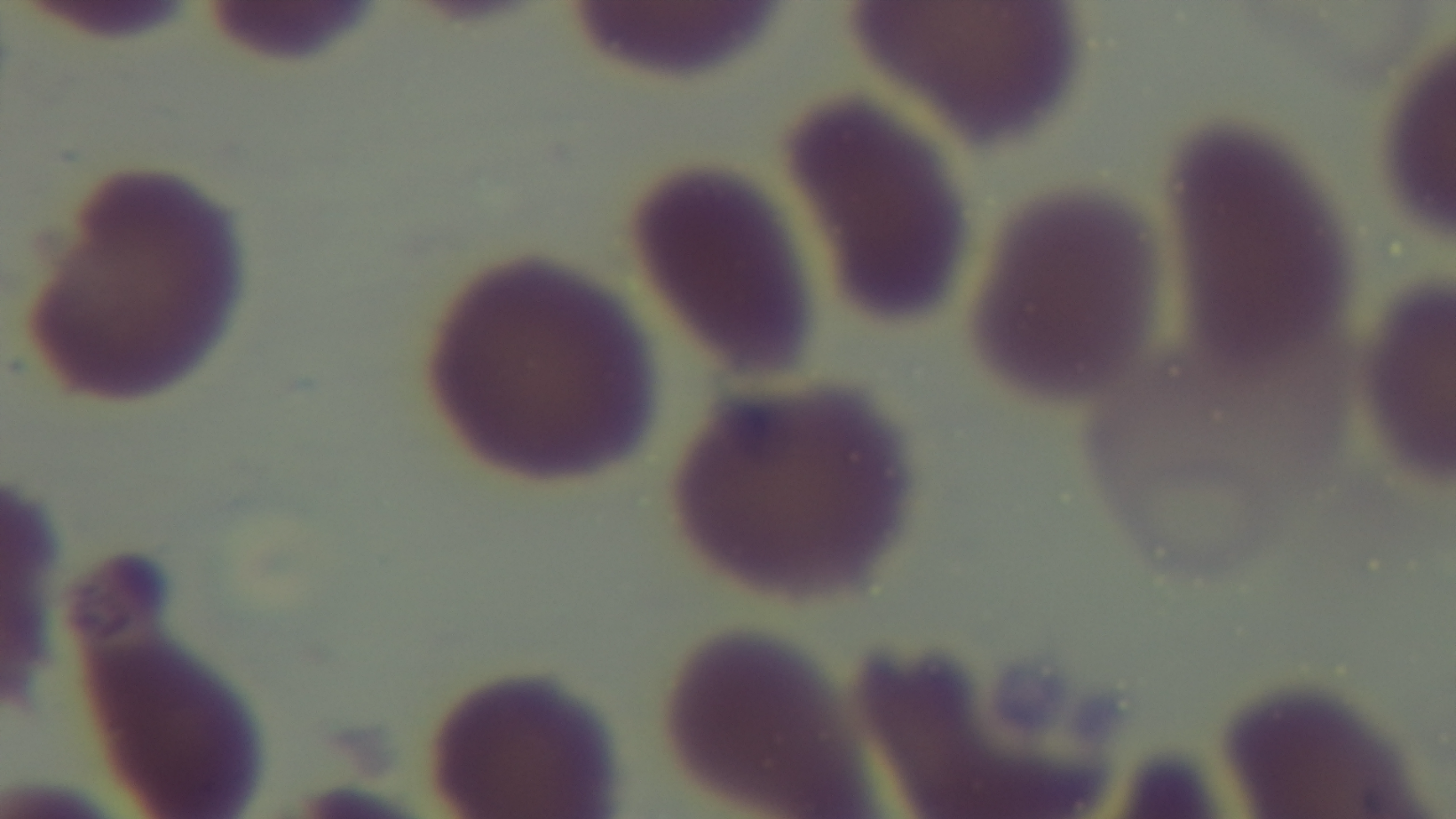
Summary:
  - Preparation: thin smear
  - Stain: Giemsa
  - Malaria status: uninfected
  - Objective: 100x oil immersion
  - Modality: light microscopy
  - Field of view: one from the slide
  - Capture: mounted 4K digital camera